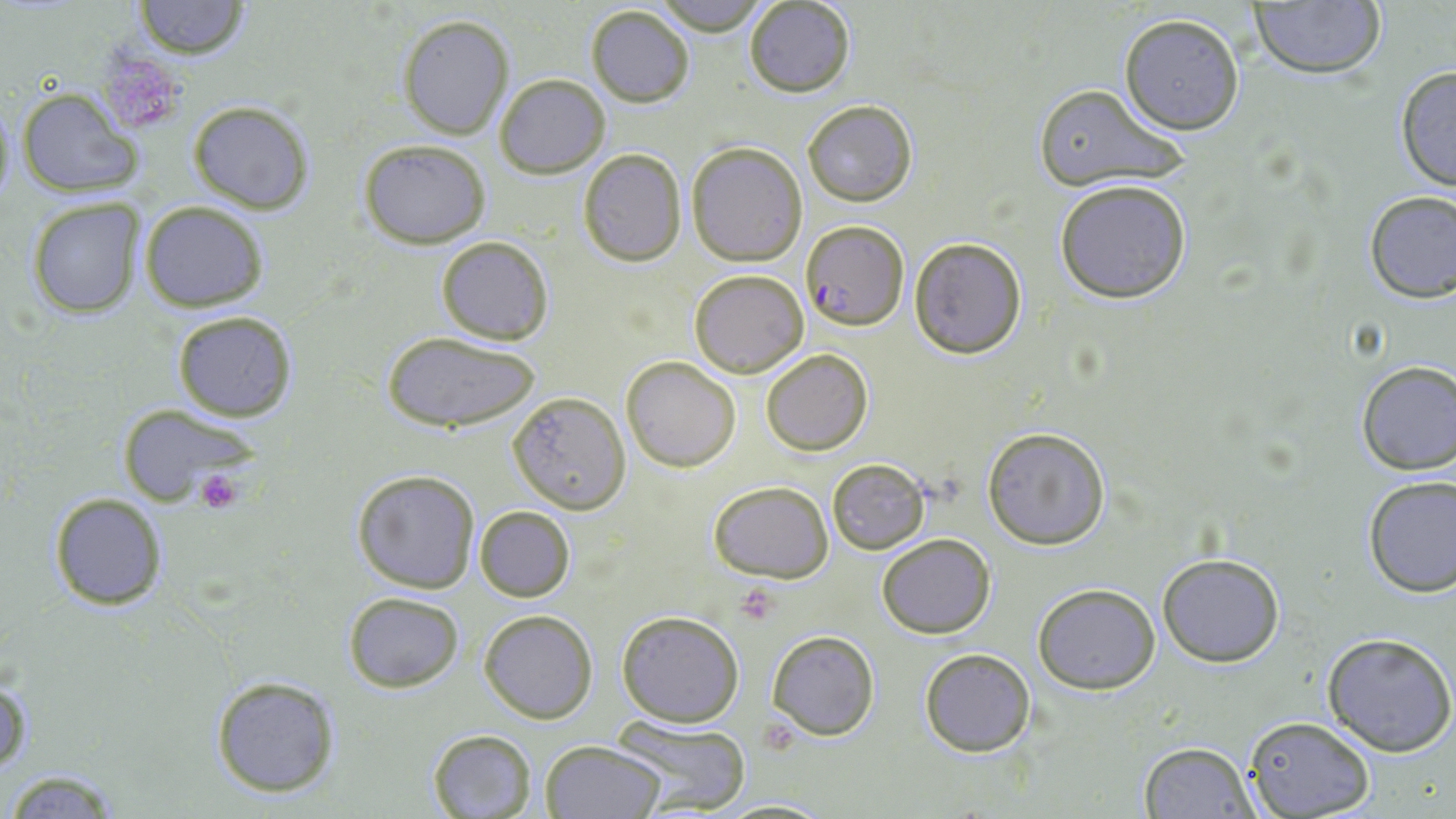
{
  "slide_level_diagnosis": "Plasmodium falciparum",
  "preparation": "thin blood film",
  "modality": "optical microscopy",
  "platelet_locations": "approximate bounding boxes as (x1, y1, x2, y2) in pixels: (93, 44, 190, 138), (191, 468, 248, 515), (734, 585, 781, 625)",
  "stain": "May-Grünwald-Giemsa",
  "uninfected_red_blood_cell_locations": "approximate bounding boxes as (x1, y1, x2, y2) in pixels: (648, 0, 774, 35), (132, 1, 250, 59), (744, 1, 856, 97), (1247, 1, 1387, 81), (585, 4, 695, 108), (1119, 13, 1246, 135), (397, 16, 514, 140), (1393, 66, 1455, 193), (495, 73, 609, 179), (1031, 84, 1188, 193), (18, 88, 143, 197), (1, 94, 17, 208), (187, 100, 315, 214), (802, 100, 918, 206), (357, 138, 492, 247), (685, 142, 809, 265), (577, 148, 686, 266), (1054, 178, 1194, 304), (1361, 189, 1455, 303), (25, 197, 147, 318), (141, 201, 268, 312), (435, 236, 555, 346), (908, 237, 1028, 358), (689, 269, 810, 379), (173, 309, 297, 422), (381, 333, 542, 432), (761, 348, 873, 456), (622, 356, 741, 473), (1354, 359, 1456, 475), (508, 391, 632, 515), (114, 402, 263, 507), (981, 427, 1110, 551), (828, 459, 930, 553), (352, 468, 481, 592), (1360, 473, 1455, 598), (708, 479, 834, 583), (47, 491, 168, 611), (474, 506, 575, 602), (877, 533, 996, 640), (1157, 553, 1285, 668), (1032, 583, 1161, 695), (342, 590, 466, 693), (479, 609, 598, 724), (616, 609, 744, 728), (767, 629, 880, 741), (1322, 631, 1455, 756), (919, 647, 1036, 756), (1, 673, 33, 778), (210, 675, 341, 798), (1243, 714, 1376, 819), (610, 717, 747, 814), (427, 728, 538, 819), (540, 740, 666, 819), (1138, 741, 1260, 818), (2, 768, 131, 817)",
  "plasmodium_falciparum_infected_red_blood_cell_locations": "approximate bounding boxes as (x1, y1, x2, y2) in pixels: (800, 220, 907, 329)",
  "magnification": "1000x",
  "image_size": "1456×819 pixels",
  "field_of_view": "one of a larger specimen"
}